Assess this cell for malaria.
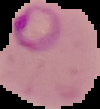
It is parasitized.

Summary:
  - Preparation: thin blood film
  - Image size: 100×109 pixels
  - Image type: segmented cell region with the area outside set to black